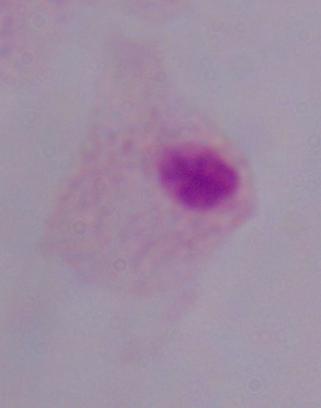

Summary:
  - Magnification: 1000x
  - Identification: trichomonad
  - Modality: micrograph